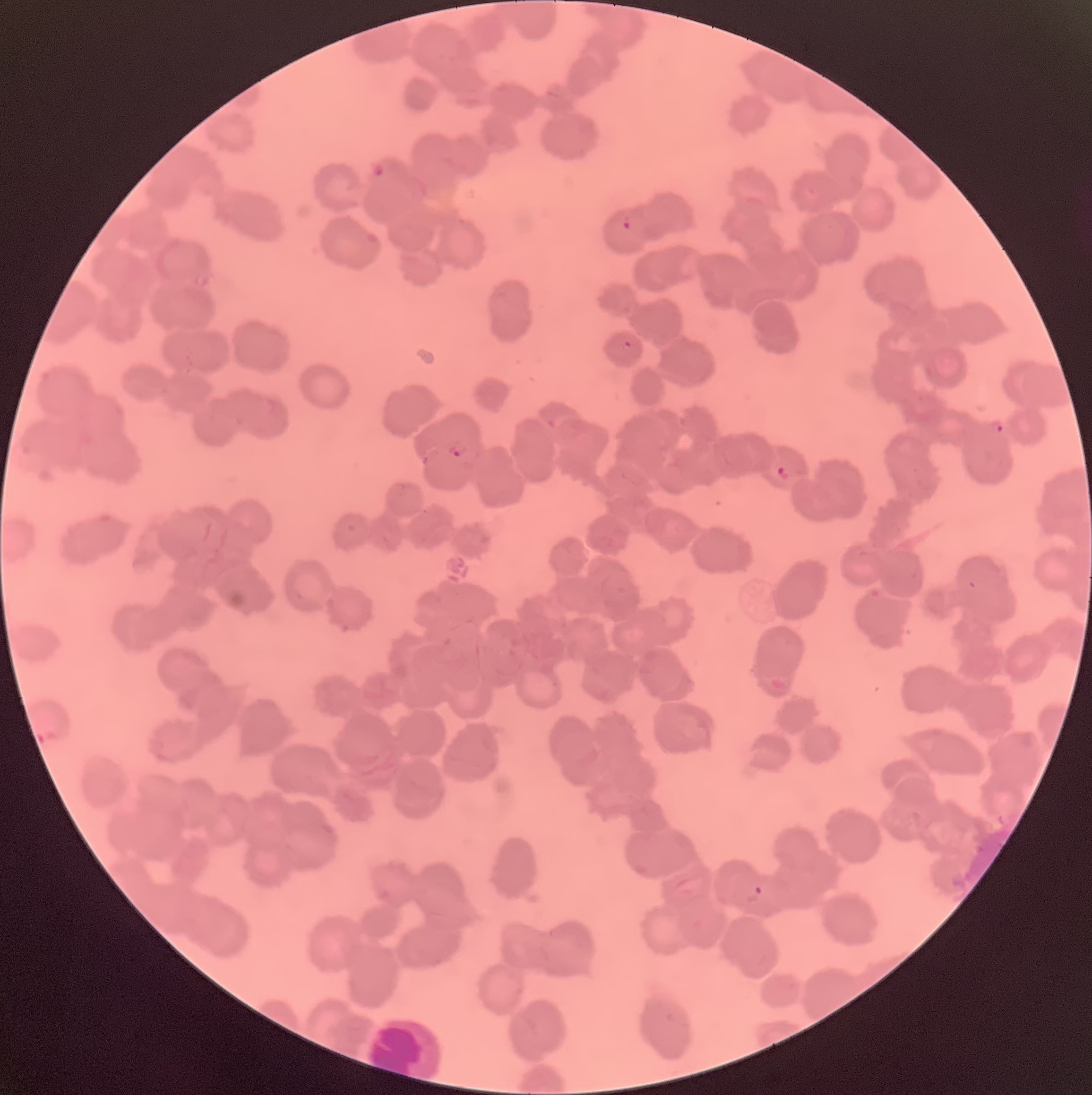
Summary:
  - Coordinate format: approximate bounding boxes as (x1, y1, x2, y2) in pixels
  - Plasmodium parasite locations: (369, 161, 387, 179), (621, 215, 633, 231), (622, 339, 633, 349), (991, 418, 1005, 435), (447, 437, 469, 459), (775, 464, 793, 482), (753, 885, 764, 899)
  - Red blood cell morphology: rouleaux formation
  - Modality: light microscopy
  - Preparation: thin blood smear
  - Image size: 1092×1095 pixels